Assess this cell for malaria.
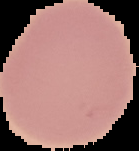
It is uninfected.

Summary:
  - Image type: segmented cell region on a black background
  - Image size: 139×151 pixels
  - Preparation: thin blood film